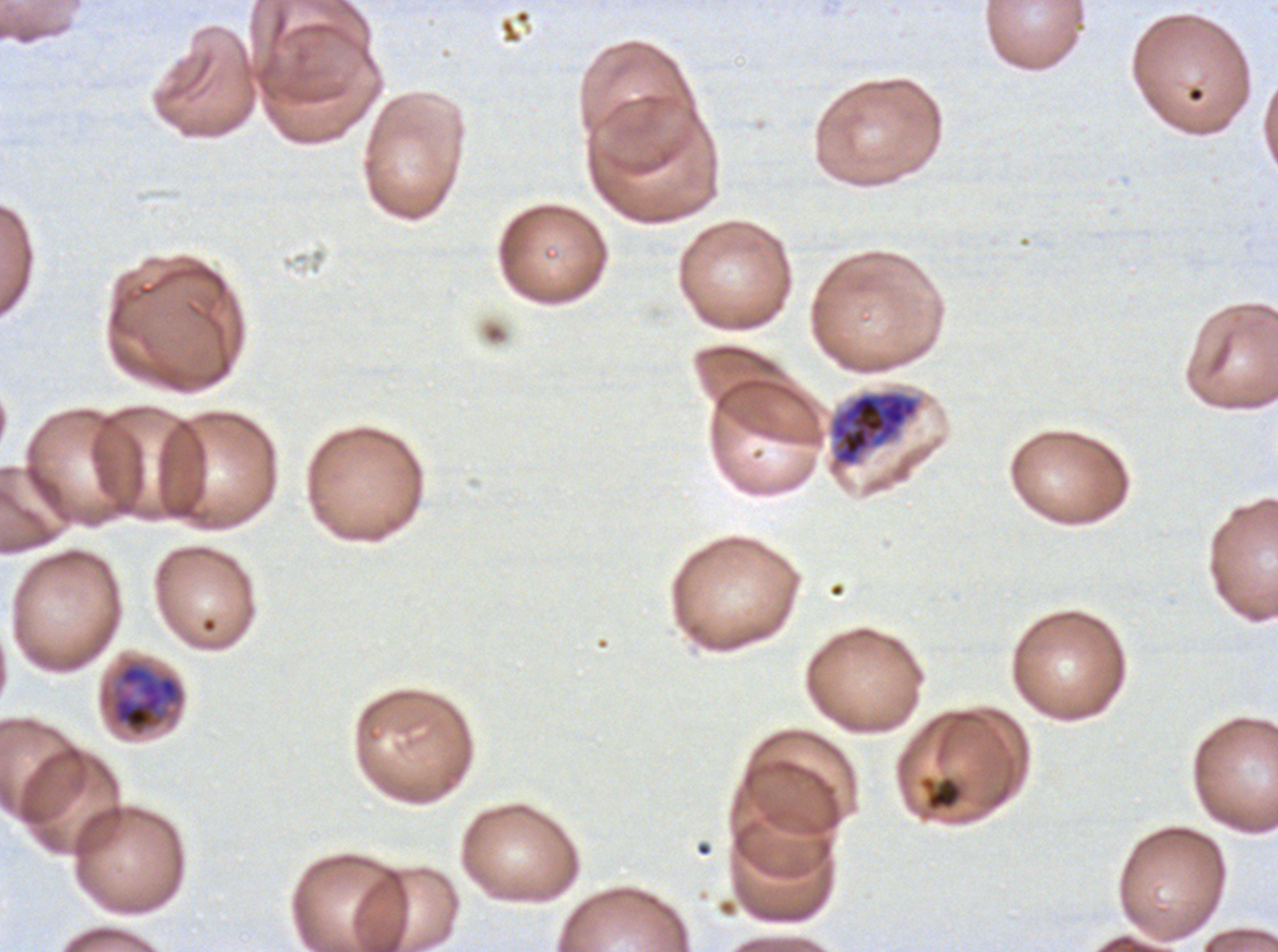

Approximate bounding rectangles given as corner coordinates in pixels from the top-left.
Summary:
  - Early schizont locations: (x1=829, y1=389, x2=921, y2=467)
  - Debris locations: (x1=918, y1=774, x2=966, y2=813)
  - Late schizont locations: (x1=99, y1=657, x2=186, y2=738)
  - Life-cycle stages observed: early schizont, late schizont
  - Image size: 1278×952 pixels
  - Preparation: thin blood film
  - Specimen: ex-vivo Plasmodium falciparum culture from a patient in The Gambia, grown for 24 to 48 hours
  - Field of view: sub-image separated from a larger composite
  - Stain: Giemsa